Point out each malaria parasite.
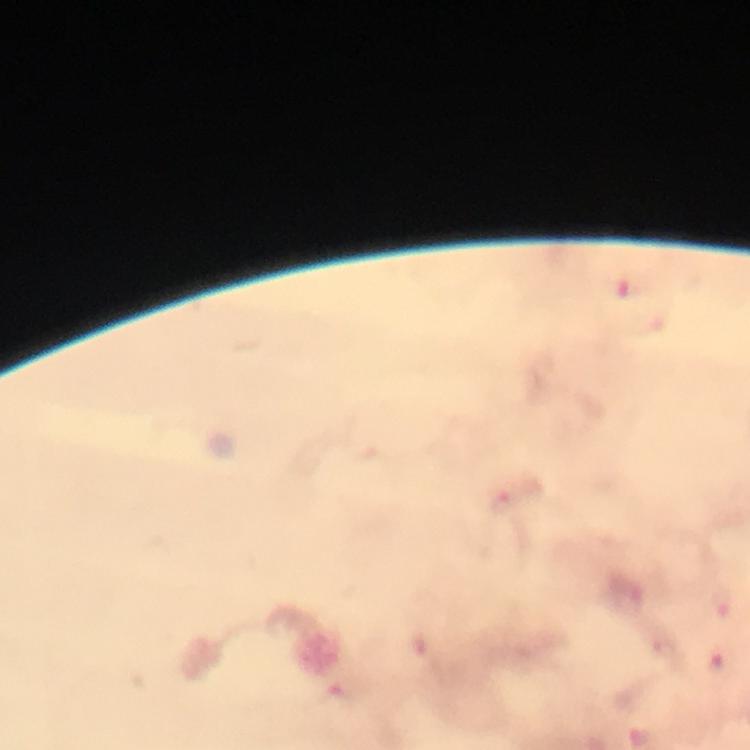
Approximate centers as [x, y] in pixels.
Malaria parasites: [632, 288], [502, 504], [666, 647], [720, 664].

Summary:
  - Context: from a diagnostic examination for malaria
  - Magnification: 100x
  - Capture: smartphone camera through the microscope
  - Stain: Giemsa
  - Preparation: thick smear
  - Immersion oil: used
  - Image size: 750×750 pixels
  - Cropped from: one field of view